Outline platelets.
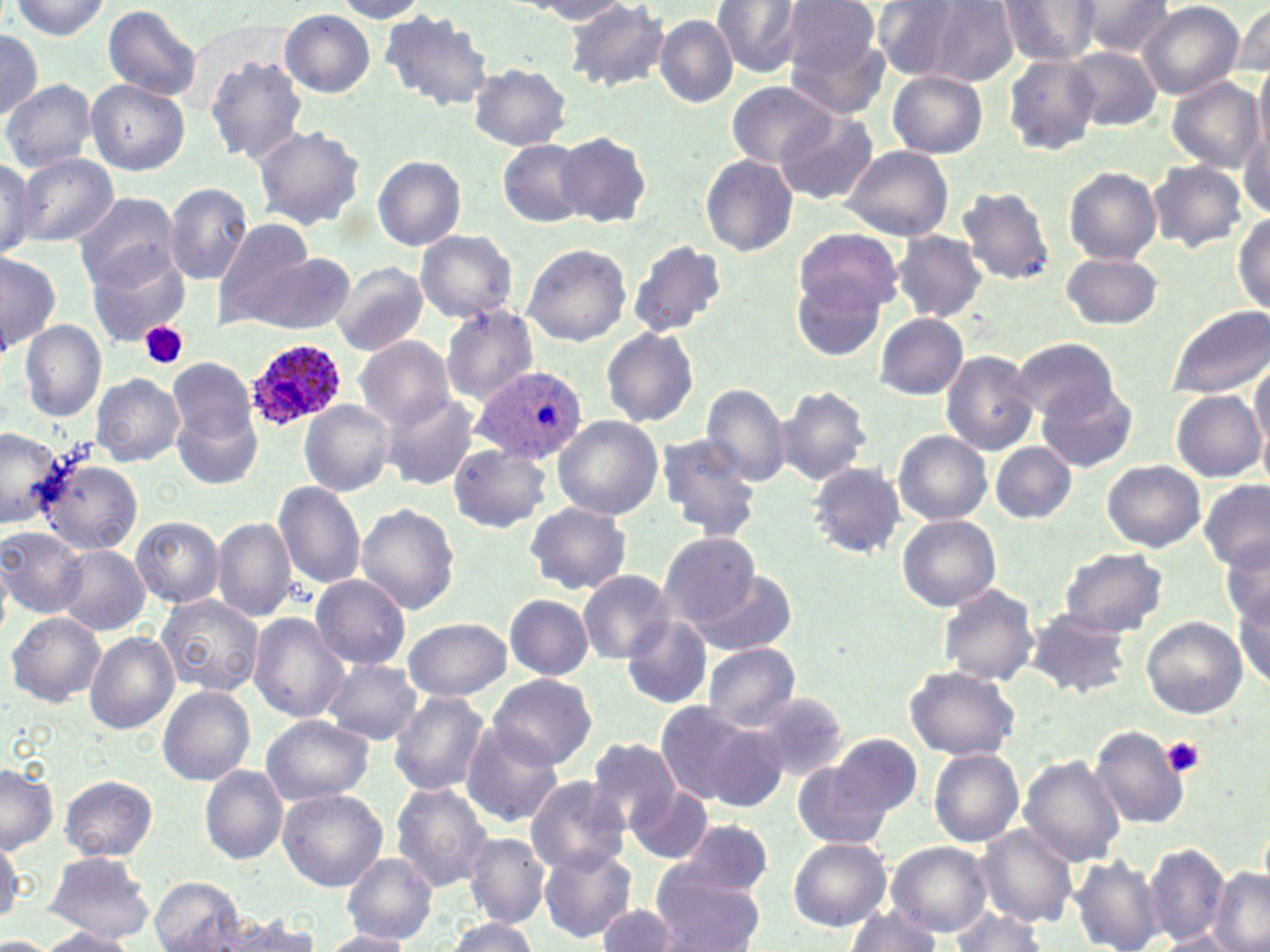
Approximate bounding boxes as (x1, y1, x2, y2) in pixels.
Platelets: (140, 321, 188, 369), (1163, 738, 1206, 776).

Uninfected red blood cell locations: (10, 0, 111, 40), (712, 0, 803, 76), (779, 0, 884, 84), (998, 0, 1103, 63), (332, 1, 430, 21), (520, 1, 638, 23), (871, 1, 987, 82), (918, 1, 1019, 86), (1074, 1, 1175, 56), (566, 2, 670, 91), (1138, 2, 1244, 100), (103, 4, 203, 102), (1232, 4, 1269, 79), (280, 9, 376, 96), (381, 9, 494, 113), (655, 15, 736, 107), (0, 28, 44, 119), (785, 28, 890, 117), (1065, 45, 1162, 131), (1001, 54, 1101, 155), (205, 56, 309, 164), (468, 63, 572, 150), (1254, 63, 1270, 164), (887, 71, 987, 158), (1168, 77, 1263, 171), (86, 79, 189, 175), (2, 81, 96, 172), (725, 83, 837, 170), (776, 111, 878, 206), (253, 125, 367, 232), (1239, 126, 1270, 221), (557, 131, 652, 230), (496, 138, 593, 228), (839, 145, 954, 241), (14, 153, 120, 247), (372, 154, 465, 251), (701, 154, 798, 257), (0, 156, 42, 257), (1149, 160, 1248, 252), (1063, 165, 1162, 265), (163, 182, 252, 283), (957, 185, 1055, 285), (71, 191, 182, 290), (1234, 212, 1269, 315), (215, 219, 318, 324), (795, 227, 902, 317), (414, 230, 519, 324), (894, 231, 987, 321), (625, 239, 726, 338), (521, 244, 631, 345), (84, 246, 192, 344), (0, 252, 60, 356), (234, 252, 357, 334), (1058, 252, 1163, 329), (329, 262, 428, 357), (791, 275, 885, 362), (440, 304, 538, 404), (1167, 304, 1270, 399), (875, 313, 970, 399), (19, 320, 106, 420), (601, 328, 699, 426), (356, 337, 456, 429), (1010, 341, 1121, 423), (940, 350, 1039, 455), (168, 356, 260, 460), (1250, 359, 1270, 451), (91, 374, 184, 465), (1037, 381, 1138, 472), (702, 383, 790, 486), (776, 384, 873, 486), (1170, 390, 1264, 481), (381, 395, 479, 491), (300, 400, 394, 496), (1256, 408, 1270, 495), (553, 415, 663, 520), (0, 425, 65, 529), (894, 431, 991, 525), (654, 433, 762, 541), (989, 442, 1077, 524), (449, 445, 550, 532), (31, 453, 146, 559), (1101, 459, 1205, 552), (807, 461, 908, 558), (273, 481, 367, 590), (1199, 481, 1269, 571), (522, 502, 632, 595), (356, 503, 461, 615), (132, 515, 224, 607), (898, 515, 1000, 612), (212, 516, 298, 623), (0, 526, 86, 618), (660, 532, 760, 626), (1221, 535, 1270, 630), (56, 544, 149, 635), (1057, 546, 1168, 636), (693, 566, 798, 657), (578, 570, 675, 662), (312, 574, 411, 669), (936, 582, 1040, 690), (1234, 589, 1269, 690), (157, 593, 266, 696), (503, 593, 594, 680), (1026, 607, 1134, 699), (247, 612, 348, 722), (7, 613, 104, 705), (621, 614, 713, 709), (1140, 616, 1248, 719), (403, 618, 512, 701), (85, 632, 180, 734), (702, 642, 800, 730), (321, 659, 422, 745), (904, 664, 1019, 760), (488, 672, 597, 770), (159, 686, 254, 784), (388, 691, 490, 795), (754, 692, 851, 783), (655, 700, 766, 805), (260, 714, 374, 804), (701, 722, 790, 808), (460, 723, 564, 827), (1090, 725, 1189, 829), (826, 732, 923, 824), (584, 736, 680, 835), (929, 748, 1025, 847), (791, 755, 902, 853), (1019, 756, 1125, 866), (0, 763, 58, 852), (199, 765, 287, 863), (59, 775, 157, 861), (525, 776, 630, 876), (390, 783, 494, 889), (626, 785, 713, 865), (278, 789, 387, 891), (674, 820, 775, 901), (978, 826, 1077, 927), (462, 833, 549, 928), (0, 836, 23, 925), (788, 838, 892, 930), (888, 842, 992, 937), (539, 845, 635, 942), (1143, 845, 1231, 946), (42, 852, 156, 943), (342, 852, 438, 945), (1072, 854, 1163, 952), (649, 869, 765, 952), (1210, 871, 1270, 952), (150, 877, 248, 952), (596, 901, 680, 951), (845, 908, 945, 951), (215, 911, 321, 952), (944, 911, 1053, 952), (443, 917, 539, 952), (37, 927, 137, 951), (319, 931, 411, 952). Plasmodium ovale-infected red blood cell locations: (243, 338, 346, 431), (469, 363, 589, 464). Slide-level diagnosis: Plasmodium ovale. 1000x magnification. Image is 1270×952 pixels. Light microscopy. Thin blood film. One field of a larger specimen. May-Grünwald-Giemsa-stained preparation.